Classify this cell by malaria status.
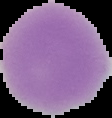
It is uninfected.

Cell region segmented out of the field of view; the surrounding area is masked to black. Image is 112×118 pixels. From a thin blood smear.